Identify the parasite.
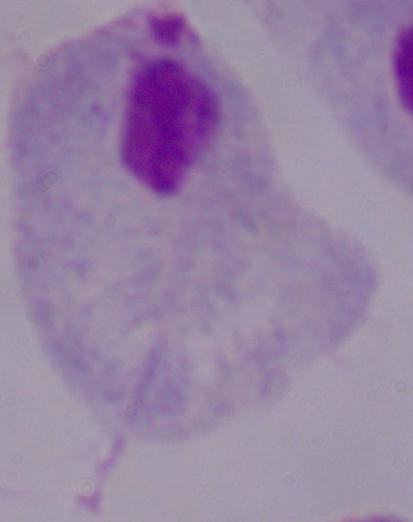
This is a trichomonad.

modality: micrograph
magnification: 1000x